Assess for Plasmodium parasites.
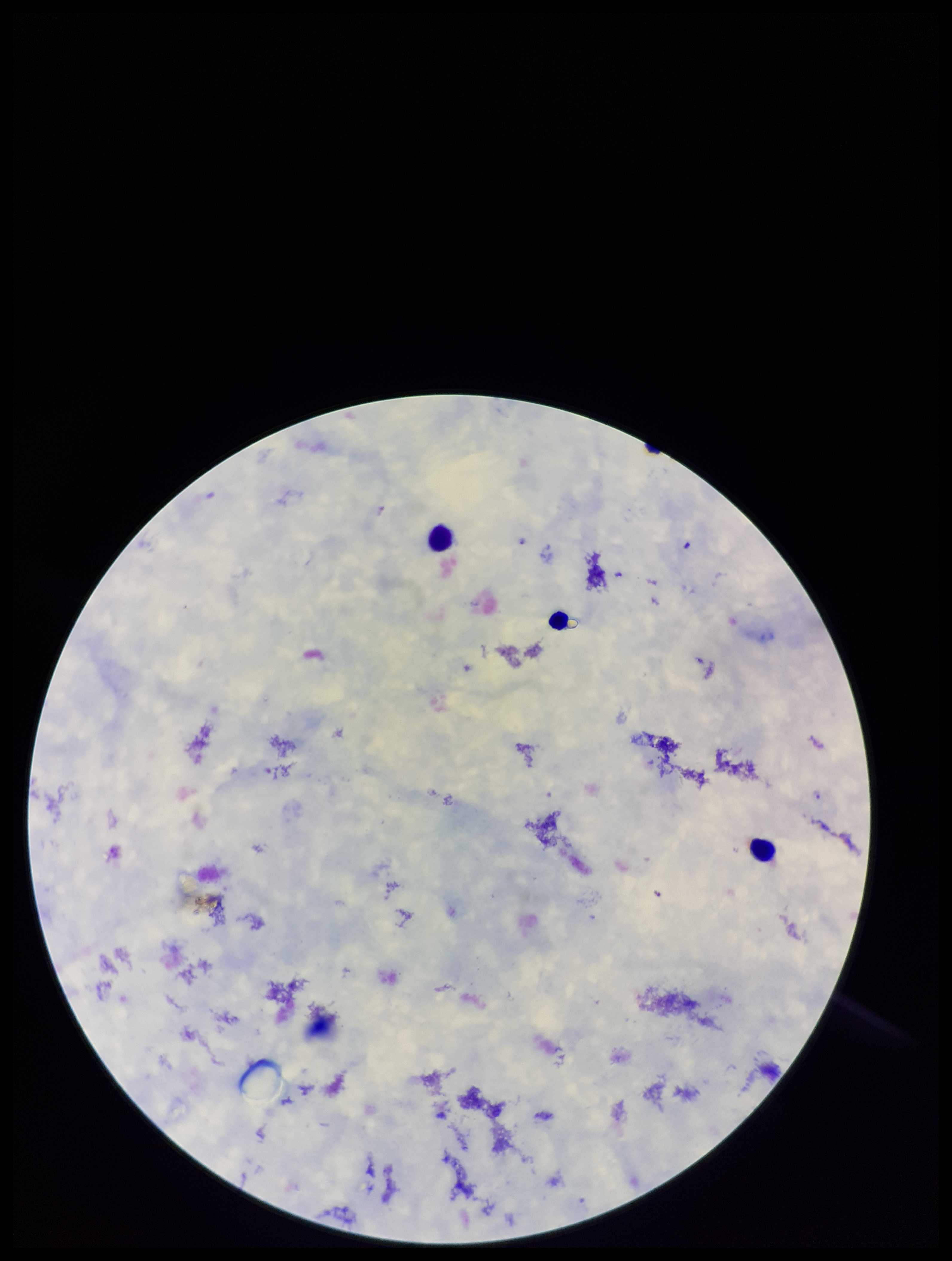
Seen.

Summary:
  - Parasite count: 3
  - Image size: 952×1261 pixels
  - Species reported for this patient: Plasmodium falciparum
  - Leukocyte count: 3
  - Stain: Giemsa
  - Patient malaria status: infected
  - Field of view: single
  - Capture: smartphone photograph through the microscope eyepiece
  - Preparation: thick blood smear